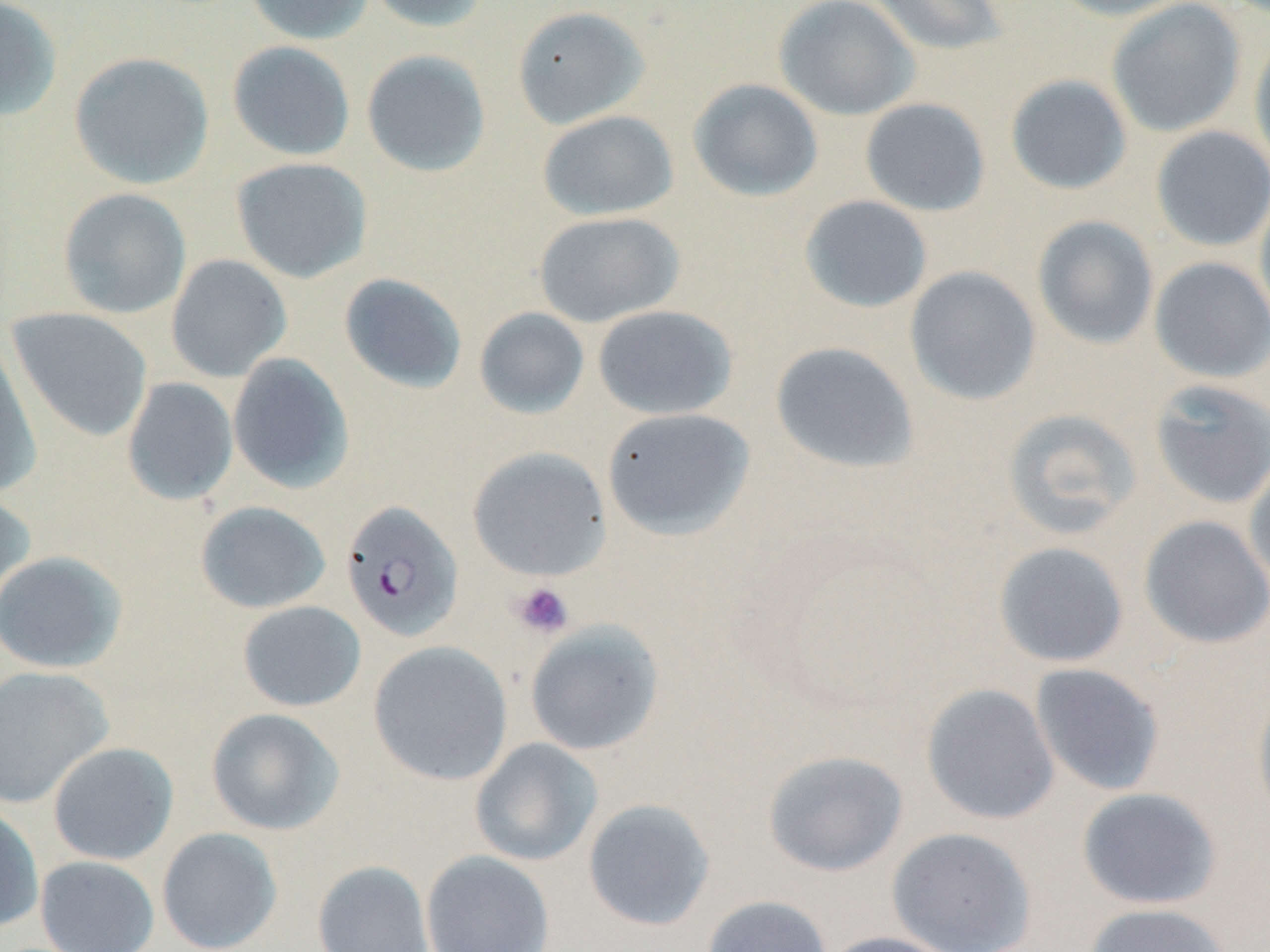
Summary:
  - Coordinate format: approximate bounding boxes as named x1/y1/x2/y2 corners in pixels
  - Uninfected red blood cell locations: (x1=0, y1=0, x2=63, y2=121), (x1=243, y1=0, x2=375, y2=45), (x1=363, y1=0, x2=493, y2=33), (x1=774, y1=0, x2=920, y2=121), (x1=866, y1=0, x2=1010, y2=58), (x1=1047, y1=0, x2=1194, y2=21), (x1=1106, y1=0, x2=1247, y2=138), (x1=511, y1=4, x2=651, y2=130), (x1=1249, y1=30, x2=1270, y2=177), (x1=226, y1=40, x2=356, y2=161), (x1=360, y1=49, x2=492, y2=178), (x1=69, y1=51, x2=215, y2=190), (x1=1005, y1=74, x2=1133, y2=195), (x1=688, y1=78, x2=823, y2=202), (x1=860, y1=98, x2=991, y2=217), (x1=537, y1=109, x2=679, y2=221), (x1=1151, y1=126, x2=1270, y2=252), (x1=231, y1=157, x2=373, y2=283), (x1=57, y1=187, x2=192, y2=320), (x1=1254, y1=187, x2=1270, y2=333), (x1=799, y1=195, x2=933, y2=314), (x1=533, y1=211, x2=685, y2=328), (x1=1032, y1=215, x2=1159, y2=349), (x1=166, y1=254, x2=292, y2=382), (x1=1149, y1=257, x2=1270, y2=383), (x1=905, y1=266, x2=1041, y2=406), (x1=338, y1=273, x2=468, y2=394), (x1=592, y1=305, x2=738, y2=420), (x1=7, y1=307, x2=153, y2=442), (x1=473, y1=307, x2=590, y2=419), (x1=0, y1=332, x2=43, y2=497), (x1=770, y1=341, x2=920, y2=475), (x1=227, y1=353, x2=355, y2=493), (x1=121, y1=377, x2=239, y2=506), (x1=1149, y1=379, x2=1270, y2=509), (x1=601, y1=407, x2=755, y2=540), (x1=1001, y1=407, x2=1143, y2=541), (x1=467, y1=446, x2=611, y2=581), (x1=1244, y1=454, x2=1270, y2=592), (x1=0, y1=489, x2=36, y2=612), (x1=194, y1=500, x2=331, y2=614), (x1=1139, y1=515, x2=1270, y2=649), (x1=993, y1=541, x2=1130, y2=668), (x1=0, y1=551, x2=129, y2=674), (x1=237, y1=600, x2=366, y2=712), (x1=524, y1=621, x2=665, y2=756), (x1=367, y1=641, x2=513, y2=786), (x1=1030, y1=663, x2=1166, y2=796), (x1=0, y1=666, x2=115, y2=808), (x1=1252, y1=682, x2=1270, y2=829), (x1=921, y1=683, x2=1060, y2=825), (x1=205, y1=707, x2=345, y2=835), (x1=469, y1=738, x2=603, y2=867), (x1=47, y1=742, x2=179, y2=865), (x1=762, y1=749, x2=909, y2=877), (x1=1076, y1=787, x2=1222, y2=910), (x1=582, y1=798, x2=715, y2=931), (x1=0, y1=803, x2=44, y2=933), (x1=886, y1=826, x2=1037, y2=952), (x1=156, y1=827, x2=283, y2=952), (x1=421, y1=849, x2=554, y2=952), (x1=35, y1=855, x2=160, y2=952), (x1=312, y1=860, x2=434, y2=952), (x1=701, y1=894, x2=833, y2=952), (x1=1083, y1=902, x2=1234, y2=952), (x1=819, y1=931, x2=962, y2=952)
  - Platelet locations: (x1=509, y1=580, x2=575, y2=639)
  - Plasmodium falciparum-infected red blood cell locations: (x1=340, y1=500, x2=464, y2=642)
  - Slide-level diagnosis: Plasmodium falciparum
  - Stain: May-Grünwald-Giemsa
  - Magnification: 1000x
  - Preparation: thin blood film
  - Modality: light microscopy
  - Field of view: single
  - Image size: 1270×952 pixels